Outline each uninfected red blood cell.
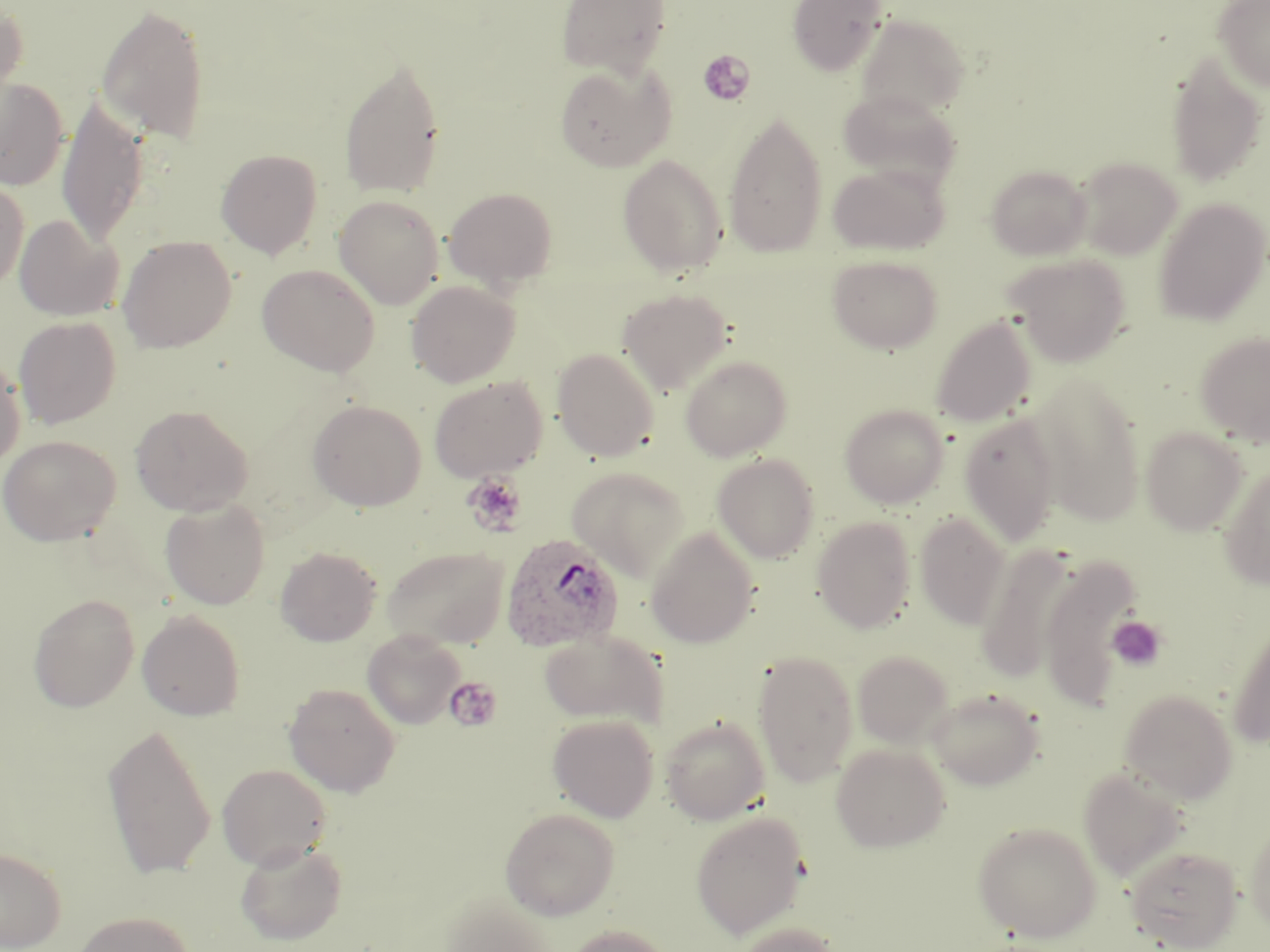

Approximate bounding boxes as (x1,y1)-(x2,y2) corner pairs in pixels.
Uninfected red blood cells: (555,0)-(672,76), (787,0)-(888,76), (1213,1)-(1270,92), (0,4)-(28,104), (95,4)-(211,144), (855,14)-(971,119), (1165,50)-(1268,188), (339,54)-(446,199), (555,62)-(676,172), (0,78)-(68,191), (838,88)-(961,189), (57,95)-(151,248), (723,110)-(828,258), (216,149)-(323,258), (617,154)-(727,278), (1074,156)-(1183,259), (828,162)-(950,256), (986,164)-(1092,260), (0,179)-(29,290), (444,187)-(558,290), (334,195)-(445,309), (1153,198)-(1270,326), (14,215)-(123,320), (117,235)-(236,353), (827,254)-(944,354), (1006,254)-(1131,366), (256,263)-(381,376), (406,279)-(520,387), (617,288)-(734,394), (931,315)-(1036,428), (14,316)-(121,429), (1195,331)-(1270,446), (552,348)-(659,461), (0,354)-(26,471), (680,354)-(792,461), (1032,372)-(1145,528), (428,375)-(548,482), (307,399)-(426,511), (840,403)-(949,508), (131,404)-(253,516), (958,413)-(1062,546), (1141,426)-(1249,535), (0,434)-(120,546), (712,453)-(820,563), (1218,462)-(1270,590), (566,467)-(691,579), (160,499)-(270,610), (914,512)-(1012,630), (812,516)-(917,633), (646,527)-(759,648), (977,543)-(1078,684), (381,545)-(510,649), (275,546)-(381,646), (1040,555)-(1141,711), (27,593)-(140,712), (137,609)-(244,721), (1226,621)-(1270,748), (362,628)-(466,728), (539,629)-(667,727), (752,650)-(858,786), (852,650)-(953,748), (284,682)-(401,797), (927,687)-(1045,790), (1119,689)-(1239,803), (547,714)-(659,822), (660,716)-(771,825), (102,720)-(217,880), (831,742)-(951,852), (216,763)-(333,869), (1079,768)-(1188,881), (500,807)-(620,920), (690,810)-(809,939), (972,821)-(1102,943), (1245,821)-(1270,932), (235,840)-(347,945), (0,846)-(67,950), (1126,846)-(1243,950), (440,893)-(557,952), (71,910)-(197,952), (731,922)-(841,952), (565,924)-(674,952).

slide_level_diagnosis: Plasmodium ovale
magnification: 1000x
field_of_view: one of a larger specimen
image_size: 1270×952 pixels
preparation: thin blood film
platelet_locations: 'approximate bounding boxes as (x1,y1)-(x2,y2) corner pairs in pixels: (697,50)-(755,107), (463,472)-(528,536), (1107,616)-(1168,671), (444,676)-(503,732)'
modality: optical microscopy
stain: May-Grünwald-Giemsa
plasmodium_ovale_infected_red_blood_cell_locations: 'approximate bounding boxes as (x1,y1)-(x2,y2) corner pairs in pixels: (500,533)-(624,652)'